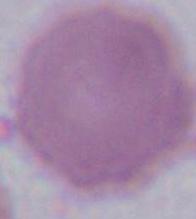

modality = micrograph
identification = red blood cell
magnification = 1000x